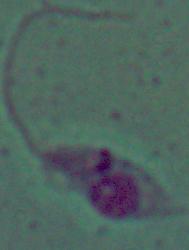
Captured at 1000x magnification. Micrograph. A Leishmania parasite is seen.